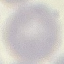
malaria_status: uninfected
stain: Giemsa
preparation: thin smear
capture: smartphone through the microscope eyepiece
image_type: cell patch, automatically extracted from a larger field of view and resized to 64 × 64 pixels